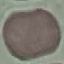
Malaria status: uninfected. Acquired by smartphone through the microscope eyepiece. Thin blood smear. Cell patch, automatically extracted from a larger field of view and resized to 64 × 64 pixels. Giemsa-stained preparation.